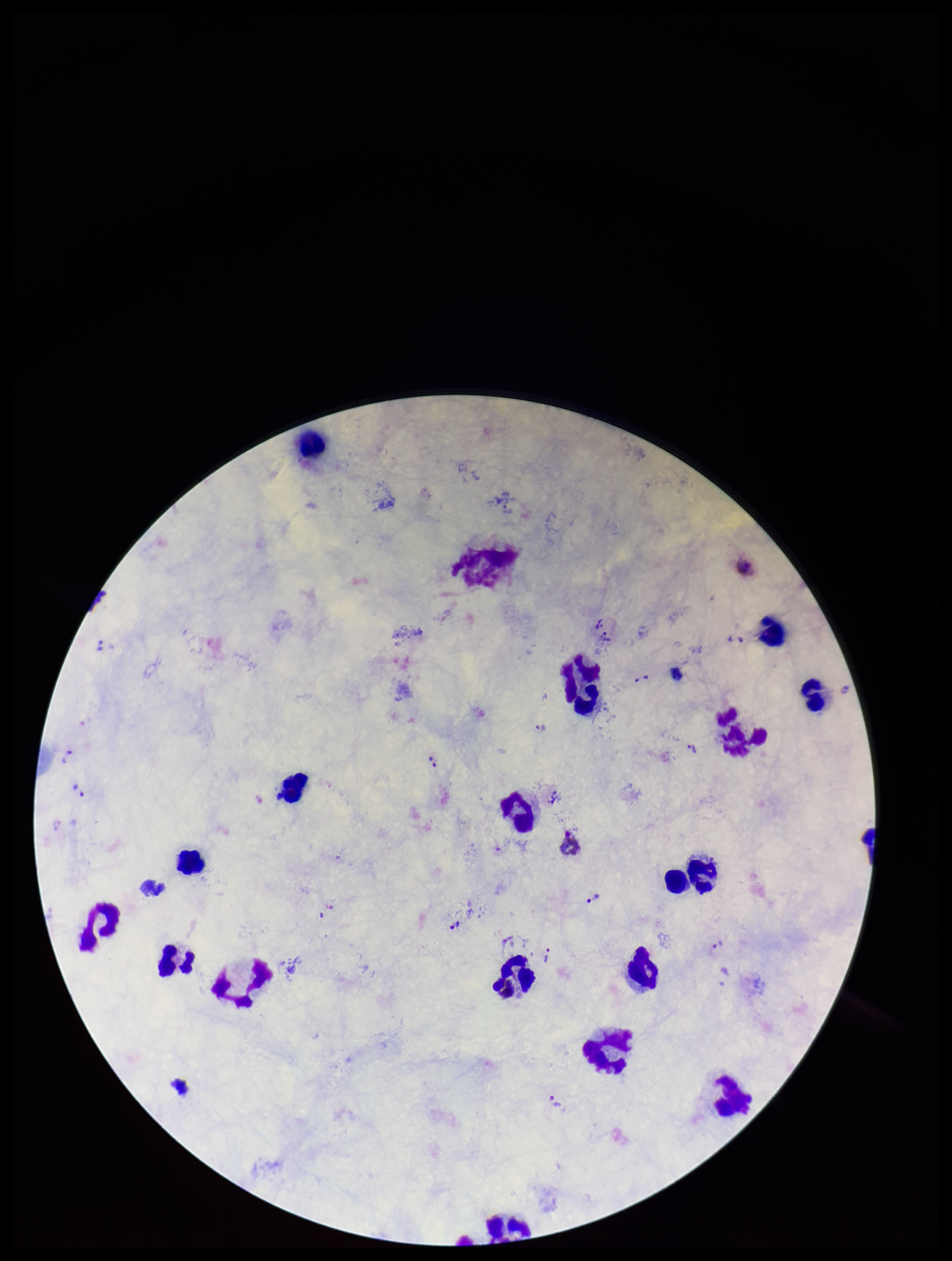
{
  "field_of_view": "one from this slide",
  "patient_malaria_status": "infected",
  "leukocyte_count": 18,
  "species_reported_for_this_patient": "Plasmodium vivax",
  "parasite_count": 19,
  "stain": "Giemsa",
  "preparation": "thick blood smear",
  "image_size": "952×1261 pixels",
  "plasmodium_parasites": "identified",
  "capture": "smartphone photograph through the microscope eyepiece"
}